Report the malaria status of this cell.
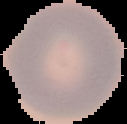
Uninfected.

Summary:
  - Preparation: thin blood film
  - Image type: segmented cell region with the area outside set to black
  - Image size: 127×124 pixels